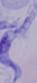 Micrograph. 1000x magnification. A trypanosome is shown.